Name the parasite shown.
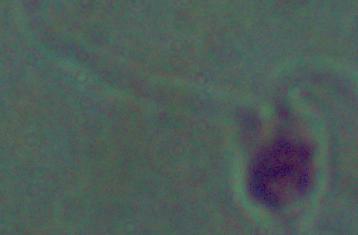

This is Leishmania.

modality = photomicrograph
magnification = 1000x